Identify the parasite.
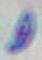

Toxoplasma gondii.

Photomicrograph. 1000x magnification.